Assess the morphology of the red blood cells.
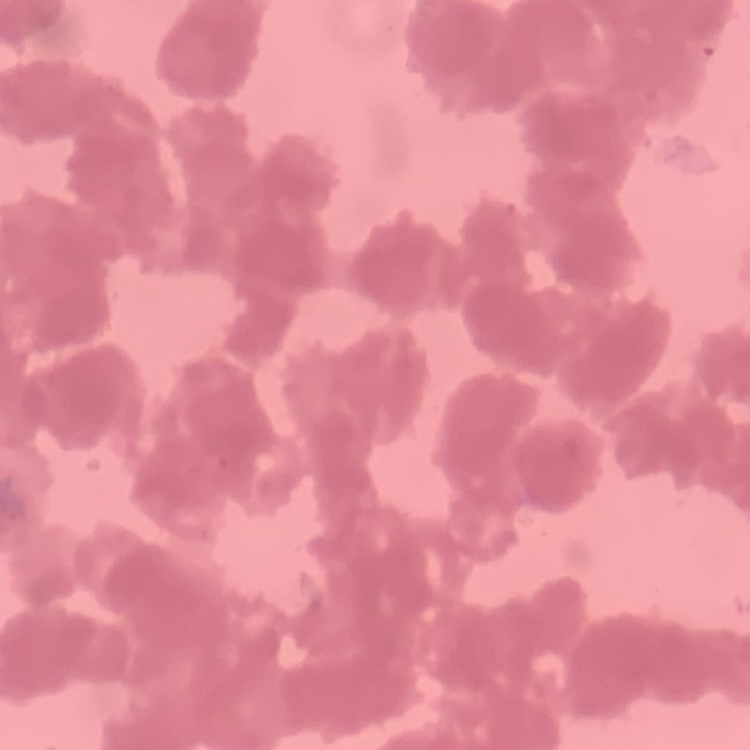

They show rouleaux formation.

Thin blood smear. Stained with either Field's or Giemsa. One tile cut from a larger photomicrograph.